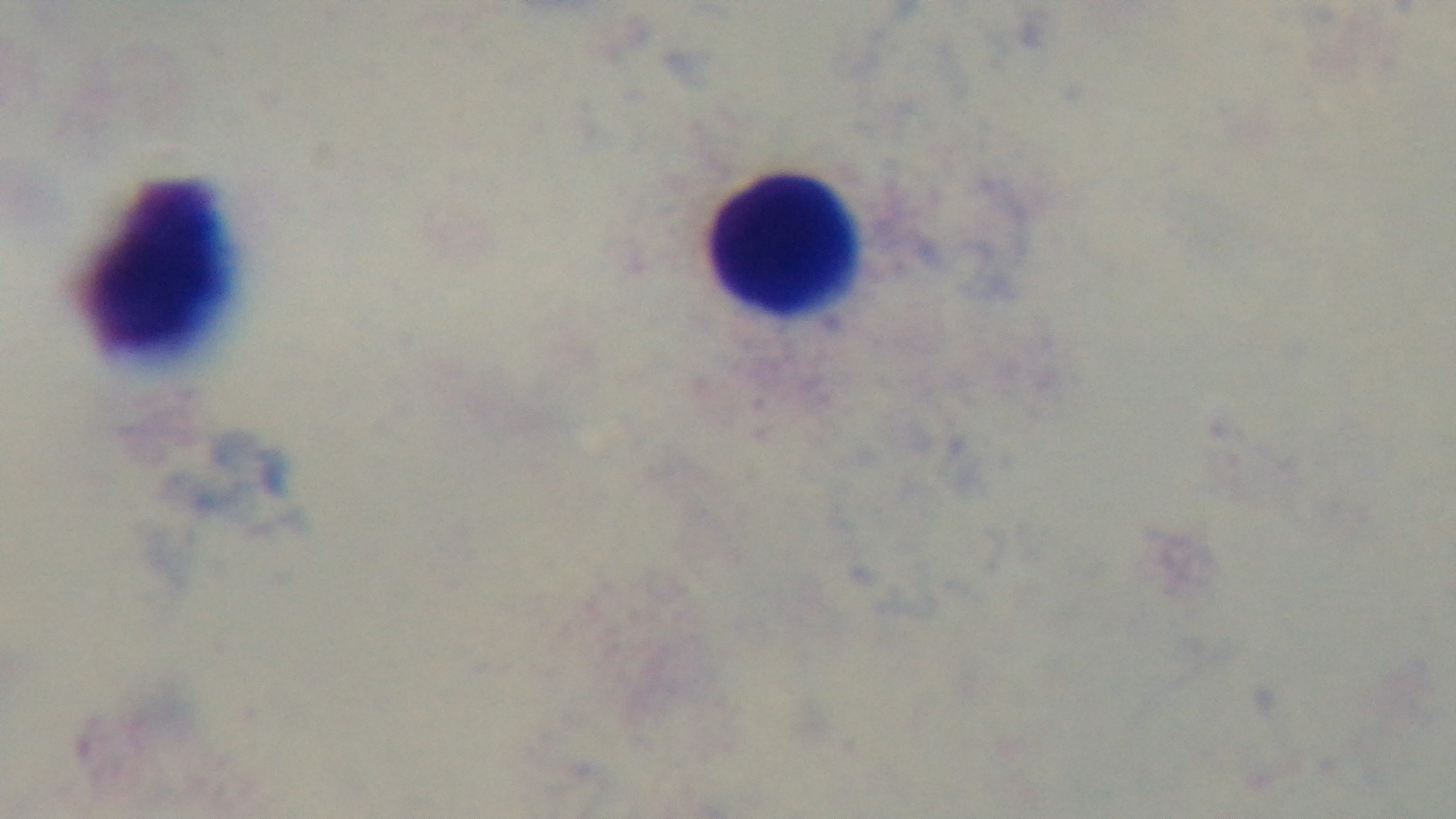 Preparation: thick blood film. Malaria status: negative. Captured with a mounted 4K digital camera. Photomicrograph. One field from the slide. 100x oil-immersion objective. Giemsa stain.